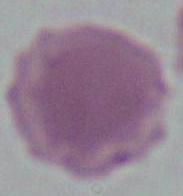 Micrograph. 1000x magnification. A red blood cell is shown.